Report the malaria status of this cell.
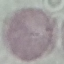

It is uninfected.

stain = Giemsa
image type = automatically extracted cell patch, resized to 64 × 64 pixels
preparation = thin smear
capture = smartphone camera at the microscope eyepiece